State the blood parasite species.
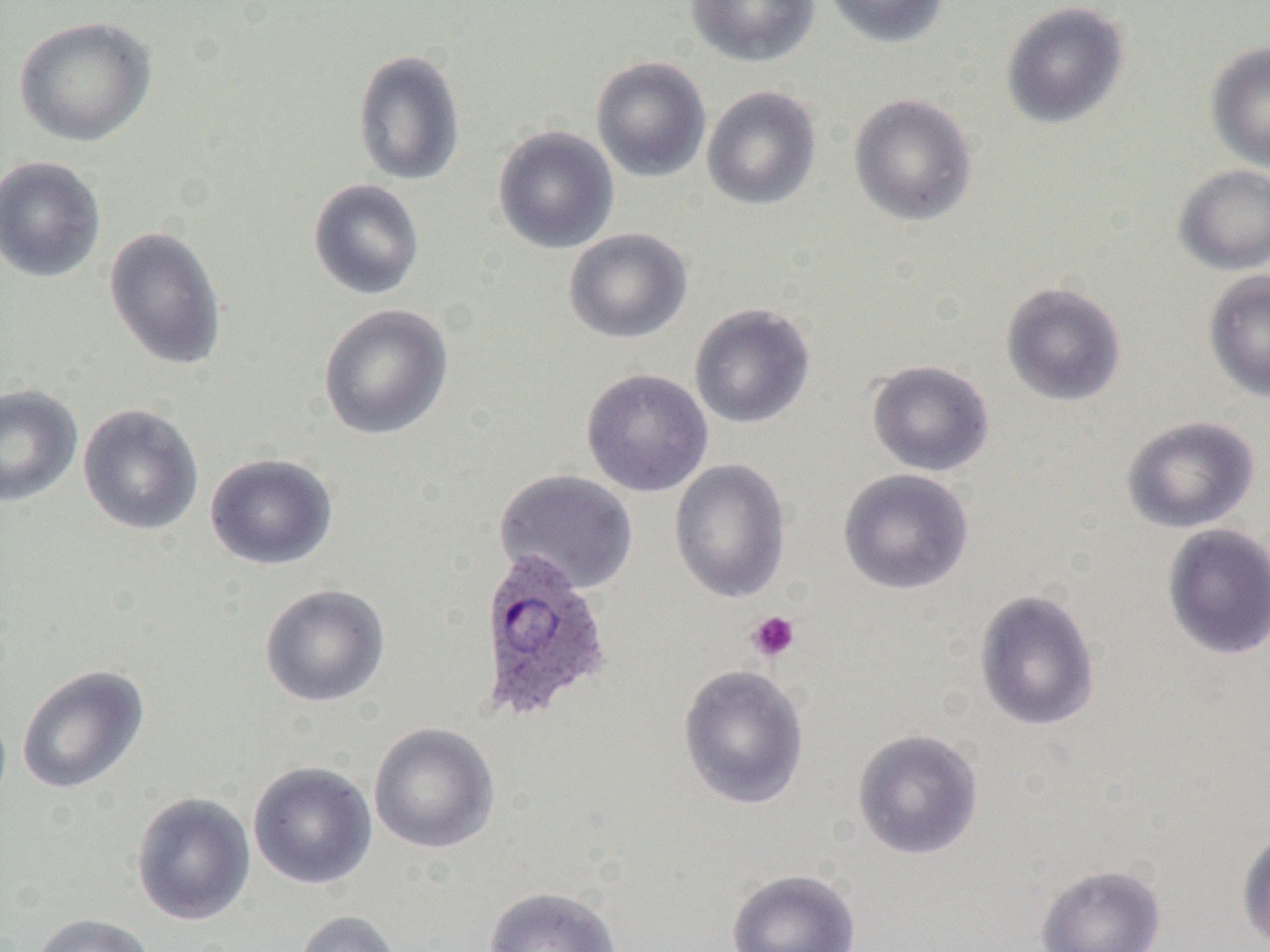

Plasmodium ovale.

platelet locations = approximate bounding boxes as (x1,y1)-(x2,y2) corner pairs in pixels: (745,610)-(801,663)
field of view = single
Plasmodium ovale-infected red blood cell locations = approximate bounding boxes as (x1,y1)-(x2,y2) corner pairs in pixels: (476,549)-(613,722)
image size = 1270×952 pixels
magnification = 1000x
modality = light microscopy
preparation = thin blood smear
uninfected red blood cell locations = approximate bounding boxes as (x1,y1)-(x2,y2) corner pairs in pixels: (685,0)-(821,66), (823,0)-(950,48), (1000,2)-(1129,129), (13,15)-(158,147), (1205,42)-(1270,173), (352,48)-(466,186), (591,56)-(711,183), (701,85)-(822,210), (848,93)-(977,227), (493,125)-(619,254), (0,155)-(106,283), (1173,164)-(1270,275), (308,178)-(425,300), (103,225)-(228,371), (564,228)-(693,344), (1203,269)-(1270,404), (1001,281)-(1127,406), (318,303)-(454,440), (689,303)-(815,429), (866,360)-(995,477), (580,368)-(713,497), (0,384)-(83,507), (77,403)-(205,536), (1121,415)-(1261,533), (205,453)-(338,570), (669,458)-(792,603), (838,468)-(975,596), (494,469)-(639,594), (1162,523)-(1270,661), (258,583)-(391,708), (974,588)-(1100,731), (16,664)-(149,795), (678,664)-(809,809), (368,722)-(500,854), (851,728)-(984,860), (247,761)-(378,890), (131,791)-(256,925), (1236,823)-(1270,951), (1034,863)-(1167,952), (726,868)-(861,952), (481,885)-(623,952), (293,910)-(402,952), (30,913)-(156,952)